Outline each white blood cell.
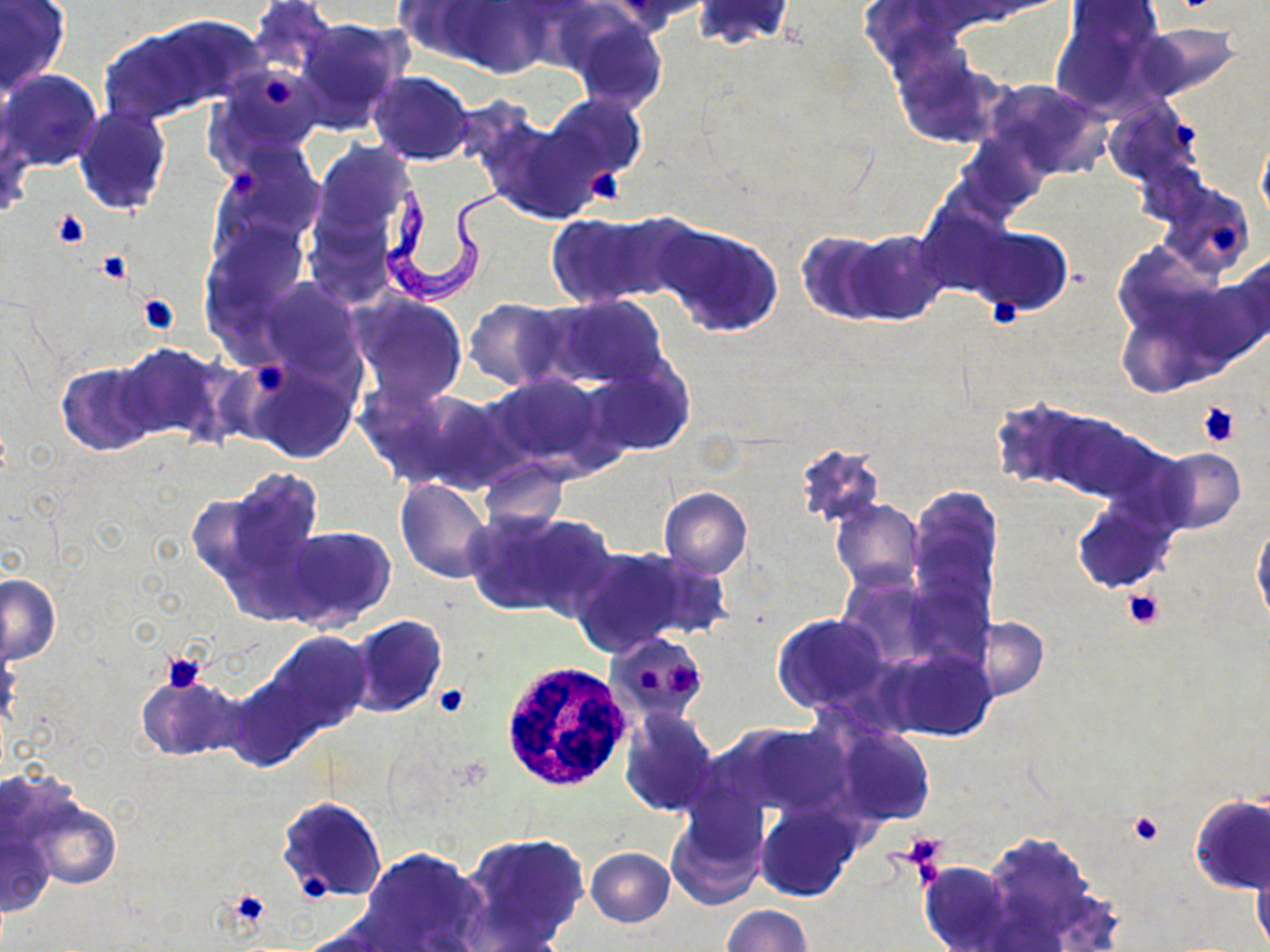

Approximate bounding boxes as (x1, y1, x2, y2) in pixels.
White blood cells: (499, 664, 630, 787).

Summary:
  - Trypanosoma brucei locations: (380, 173, 524, 307)
  - Uninfected red blood cell locations: (249, 0, 337, 82), (392, 0, 499, 63), (608, 0, 709, 33), (443, 1, 551, 77), (692, 1, 795, 51), (0, 2, 69, 95), (1050, 5, 1163, 117), (560, 8, 669, 111), (292, 17, 411, 132), (99, 21, 220, 124), (1131, 24, 1247, 102), (894, 50, 996, 143), (213, 68, 323, 165), (2, 69, 102, 172), (367, 71, 475, 165), (983, 80, 1110, 178), (542, 94, 645, 182), (1103, 100, 1199, 188), (73, 105, 171, 217), (1256, 131, 1270, 225), (962, 133, 1046, 215), (305, 141, 420, 272), (222, 149, 323, 243), (1156, 181, 1255, 279), (546, 212, 679, 308), (207, 221, 306, 322), (652, 221, 785, 338), (970, 227, 1071, 317), (843, 230, 949, 325), (793, 231, 894, 325), (1203, 256, 1270, 364), (260, 279, 360, 376), (350, 293, 469, 410), (541, 296, 668, 390), (464, 298, 572, 389), (1119, 310, 1201, 396), (112, 343, 230, 446), (244, 358, 360, 463), (588, 361, 694, 456), (56, 362, 156, 455), (484, 372, 615, 474), (368, 384, 512, 495), (988, 401, 1094, 491), (1037, 406, 1159, 502), (792, 443, 886, 529), (1153, 449, 1245, 533), (478, 458, 569, 533), (201, 467, 326, 604), (394, 478, 492, 583), (659, 487, 752, 578), (908, 488, 1003, 610), (831, 499, 923, 594), (1072, 502, 1174, 593), (464, 509, 608, 620), (1251, 523, 1269, 627), (280, 524, 396, 632), (569, 548, 704, 656), (837, 573, 949, 671), (1, 574, 61, 665), (772, 613, 889, 713), (347, 614, 447, 716), (972, 617, 1047, 700), (260, 632, 371, 739), (605, 632, 710, 722), (883, 647, 999, 741), (134, 674, 243, 761), (619, 708, 720, 817), (731, 723, 851, 814), (833, 726, 936, 828), (1190, 794, 1270, 895), (21, 796, 120, 891), (278, 796, 387, 902), (666, 799, 769, 910), (756, 803, 862, 902), (2, 828, 53, 914), (460, 833, 589, 951), (978, 834, 1109, 943), (359, 846, 486, 952), (585, 847, 675, 927), (1249, 851, 1270, 951), (919, 862, 1013, 951), (722, 905, 810, 952)
  - Platelet locations: (262, 75, 293, 106), (1172, 121, 1197, 148), (229, 169, 262, 194), (585, 170, 630, 207), (52, 209, 91, 248), (1208, 223, 1242, 254), (96, 249, 132, 284), (136, 293, 179, 335), (990, 298, 1018, 326), (250, 358, 293, 398), (1196, 401, 1240, 448), (1121, 587, 1165, 628), (160, 650, 207, 694), (663, 661, 701, 697), (638, 664, 661, 694), (433, 684, 468, 716), (1130, 811, 1165, 845), (901, 831, 948, 871), (302, 873, 330, 896), (225, 889, 269, 929)
  - Slide-level diagnosis: Trypanosoma brucei
  - Modality: light microscopy
  - Preparation: thin blood smear
  - Image size: 1270×952 pixels
  - Stain: May-Grünwald-Giemsa
  - Magnification: 1000x
  - Field of view: single